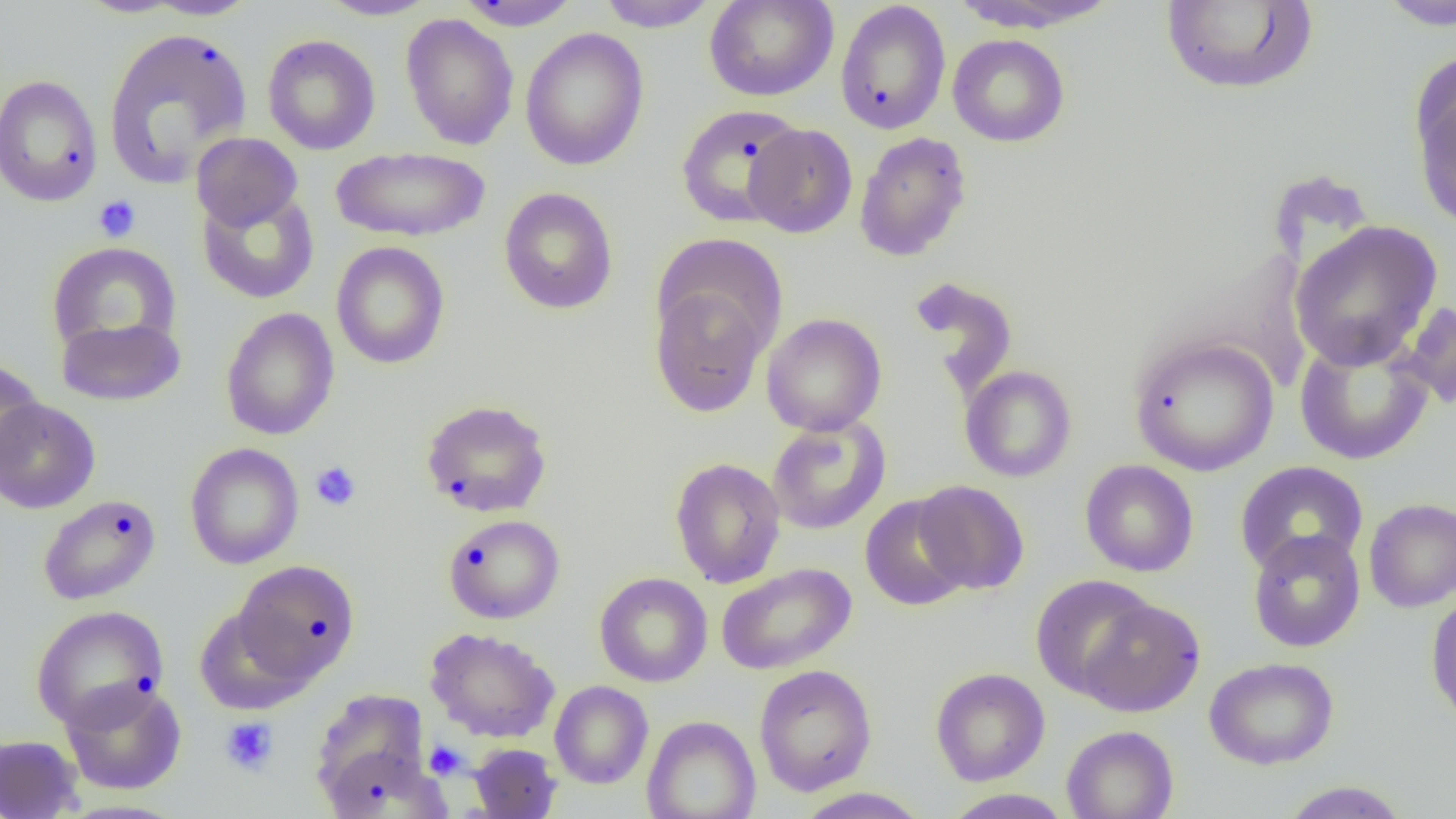

Summary:
  - Coordinate format: approximate bounding boxes as (x1, y1, x2, y2) in pixels
  - Platelet locations: (93, 195, 141, 242), (310, 461, 362, 511), (220, 717, 278, 776), (424, 740, 467, 779)
  - Uninfected red blood cell locations: (75, 0, 190, 18), (143, 0, 261, 20), (318, 0, 440, 20), (455, 0, 582, 31), (595, 0, 719, 31), (704, 0, 838, 102), (951, 0, 1121, 33), (1161, 0, 1319, 96), (835, 1, 951, 135), (1376, 1, 1456, 31), (400, 14, 519, 150), (103, 27, 252, 188), (520, 27, 649, 171), (947, 33, 1070, 147), (263, 34, 381, 154), (0, 74, 103, 208), (1413, 75, 1456, 232), (675, 103, 806, 228), (744, 123, 858, 238), (191, 132, 303, 232), (854, 132, 972, 262), (331, 145, 490, 243), (498, 187, 618, 315), (197, 188, 319, 304), (1288, 220, 1443, 371), (46, 241, 182, 356), (331, 241, 450, 369), (909, 276, 1018, 394), (650, 283, 771, 418), (1396, 299, 1456, 411), (220, 307, 339, 440), (761, 313, 887, 436), (55, 315, 187, 407), (1294, 334, 1434, 466), (1129, 335, 1279, 476), (0, 359, 45, 478), (960, 365, 1077, 482), (0, 397, 101, 514), (420, 399, 553, 517), (766, 416, 891, 535), (185, 443, 304, 570), (669, 457, 786, 588), (1080, 460, 1199, 577), (1234, 461, 1369, 577), (914, 481, 1029, 595), (38, 493, 161, 605), (860, 495, 971, 611), (1363, 498, 1456, 612), (444, 514, 565, 624), (1247, 528, 1365, 653), (232, 559, 360, 685), (716, 563, 857, 675), (594, 572, 712, 687), (1030, 575, 1158, 699), (1425, 592, 1456, 727), (1075, 596, 1205, 717), (30, 604, 169, 731), (194, 607, 311, 714), (425, 627, 561, 742), (1204, 657, 1339, 770), (753, 664, 877, 796), (930, 667, 1050, 786), (59, 679, 187, 795), (549, 680, 653, 788), (311, 695, 438, 813), (641, 715, 761, 819), (1061, 725, 1178, 819), (0, 734, 83, 819), (469, 743, 562, 818), (1278, 781, 1412, 818), (793, 787, 930, 818), (941, 788, 1074, 819)
  - Slide-level diagnosis: negative for blood parasites
  - Modality: optical microscopy
  - Field of view: single
  - Preparation: thin blood smear
  - Image size: 1456×819 pixels
  - Magnification: 1000x